Identify the parasite.
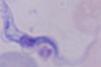
A trypanosome.

Summary:
  - Modality: micrograph
  - Magnification: 1000x